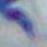
identification = Toxoplasma gondii
magnification = 1000x
modality = micrograph